Assess this cell for malaria.
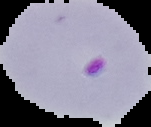
Parasitized.

Summary:
  - Preparation: thin blood film
  - Image size: 151×127 pixels
  - Image type: segmented cell region on a black background